Locate every Plasmodium parasite.
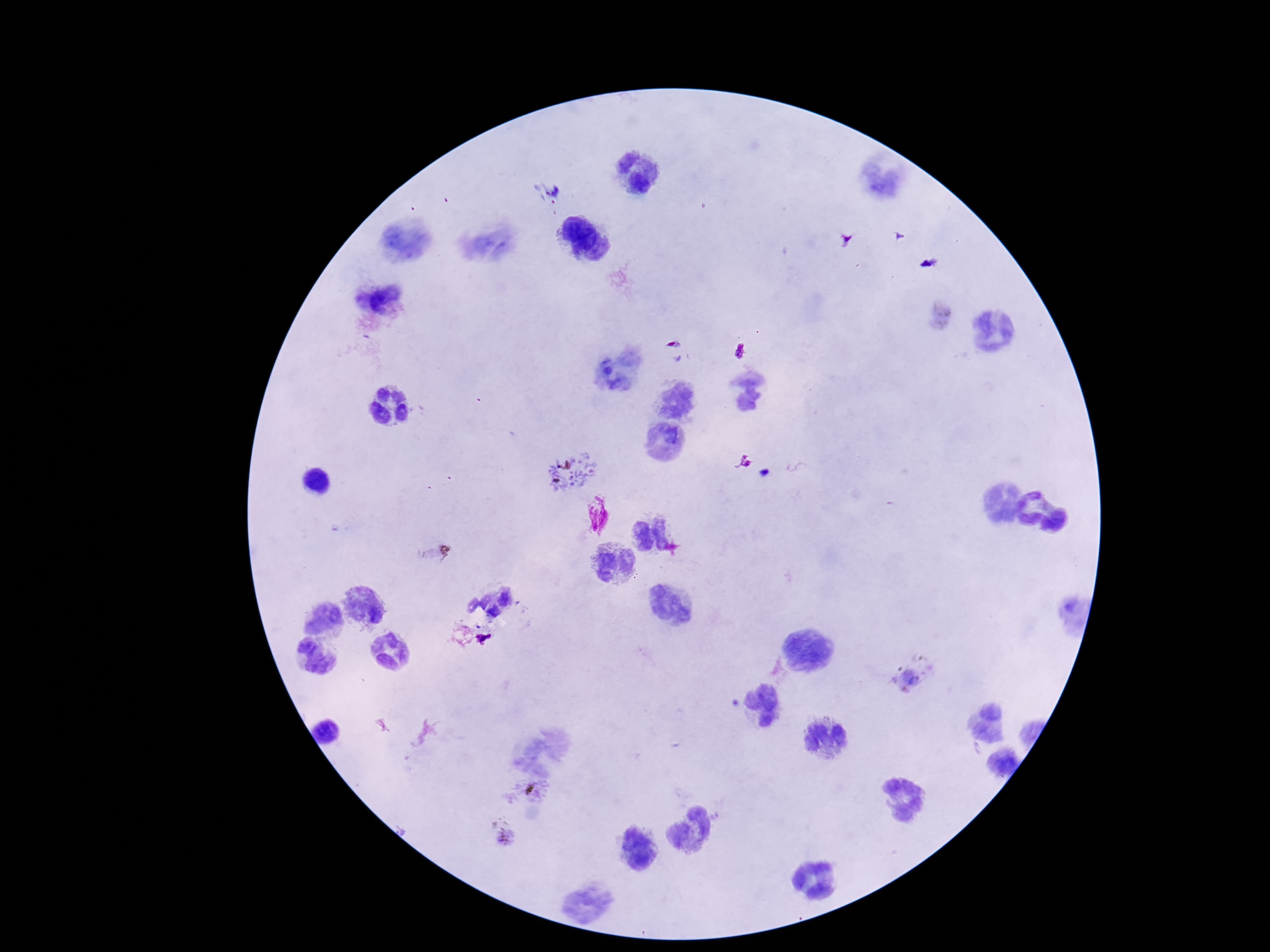

Approximate object centers, in pixels from the top-left corner.
Plasmodium parasites: (x=570, y=469), (x=912, y=677), (x=528, y=787), (x=504, y=831).

capture = smartphone camera through the microscope eyepiece
preparation = thick peripheral-blood smear
stain = Giemsa
image size = 1270×952 pixels
patient malaria status = infected
magnification = 100x
field of view = one from this slide